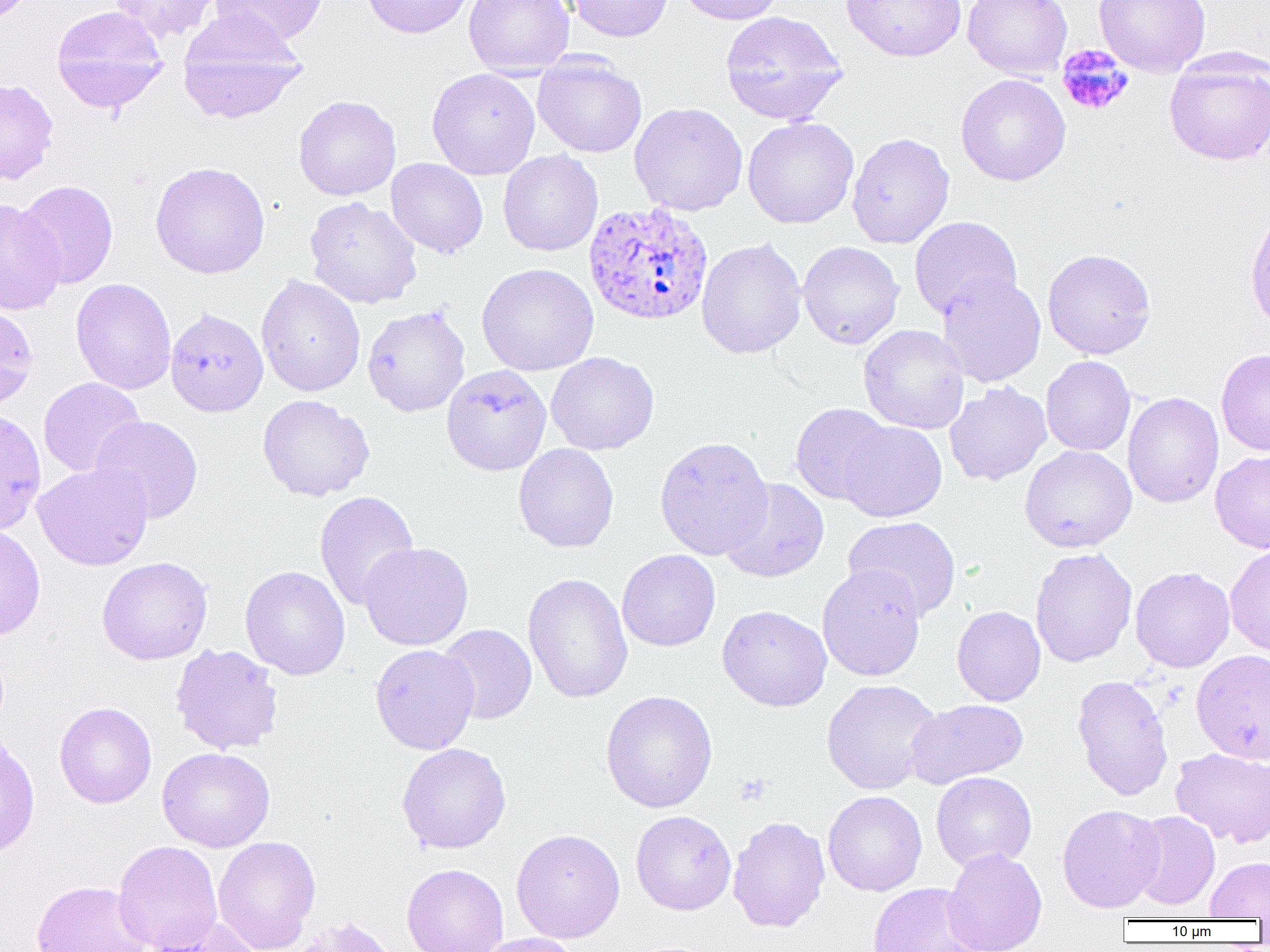
Summary:
  - Coordinate format: approximate bounding boxes as (x1,y1)-(x2,y2) corner pairs in pixels
  - Uninfected red blood cell locations: (110,0)-(222,43), (210,0)-(329,48), (360,0)-(474,39), (464,0)-(575,78), (567,0)-(673,42), (677,0)-(785,25), (841,0)-(967,62), (963,0)-(1072,81), (1093,0)-(1211,77), (50,5)-(169,113), (179,9)-(308,125), (719,10)-(848,125), (532,54)-(647,158), (1163,55)-(1270,166), (427,68)-(540,179), (956,74)-(1071,186), (0,78)-(59,185), (293,95)-(400,201), (629,102)-(748,216), (742,116)-(859,229), (847,132)-(955,248), (498,150)-(603,256), (386,158)-(488,258), (150,161)-(271,279), (16,180)-(118,289), (305,196)-(422,308), (0,198)-(65,316), (909,216)-(1022,320), (696,238)-(806,359), (797,241)-(904,349), (1042,248)-(1156,359), (477,263)-(599,375), (937,272)-(1046,388), (256,274)-(366,397), (71,278)-(177,395), (0,304)-(39,411), (362,305)-(470,417), (165,307)-(268,417), (859,324)-(969,434), (1216,348)-(1270,456), (546,352)-(659,455), (1041,356)-(1136,456), (441,365)-(551,476), (38,377)-(146,478), (944,381)-(1051,486), (1122,392)-(1224,508), (257,394)-(374,502), (790,403)-(894,505), (89,415)-(203,524), (837,421)-(947,522), (654,435)-(774,560), (513,443)-(619,553), (1020,445)-(1136,552), (1210,450)-(1270,553), (32,463)-(153,571), (719,479)-(830,583), (314,491)-(419,611), (843,516)-(961,620), (0,523)-(46,641), (359,542)-(474,651), (1224,543)-(1270,657), (1030,547)-(1137,667), (617,550)-(720,652), (96,556)-(213,665), (817,564)-(926,681), (240,565)-(350,680), (1130,566)-(1235,672), (522,572)-(634,704), (717,605)-(832,712), (952,605)-(1046,706), (437,624)-(537,724), (169,644)-(284,755), (370,644)-(480,754), (1191,650)-(1270,763), (1072,674)-(1174,801), (821,679)-(941,794), (600,690)-(718,813), (906,699)-(1028,788), (54,701)-(156,808), (0,735)-(40,858), (396,742)-(511,853), (156,747)-(275,852), (1171,748)-(1270,847), (931,771)-(1037,871), (823,790)-(927,896), (1057,804)-(1165,912), (630,810)-(736,915), (1128,811)-(1220,911), (728,816)-(831,933), (511,828)-(625,943), (212,836)-(321,952), (113,840)-(222,952), (943,848)-(1047,952), (1205,856)-(1270,920), (401,863)-(509,952), (31,880)-(152,952), (867,882)-(987,951), (145,916)-(264,952), (286,916)-(398,952), (473,933)-(581,952)
  - Platelet locations: (1056,44)-(1135,116), (735,774)-(771,806)
  - Plasmodium ovale-infected red blood cell locations: (584,202)-(713,326)
  - Slide-level diagnosis: Plasmodium ovale
  - Modality: light microscopy
  - Field of view: one of a larger specimen
  - Preparation: thin blood smear
  - Magnification: 1000x
  - Image size: 1270×952 pixels